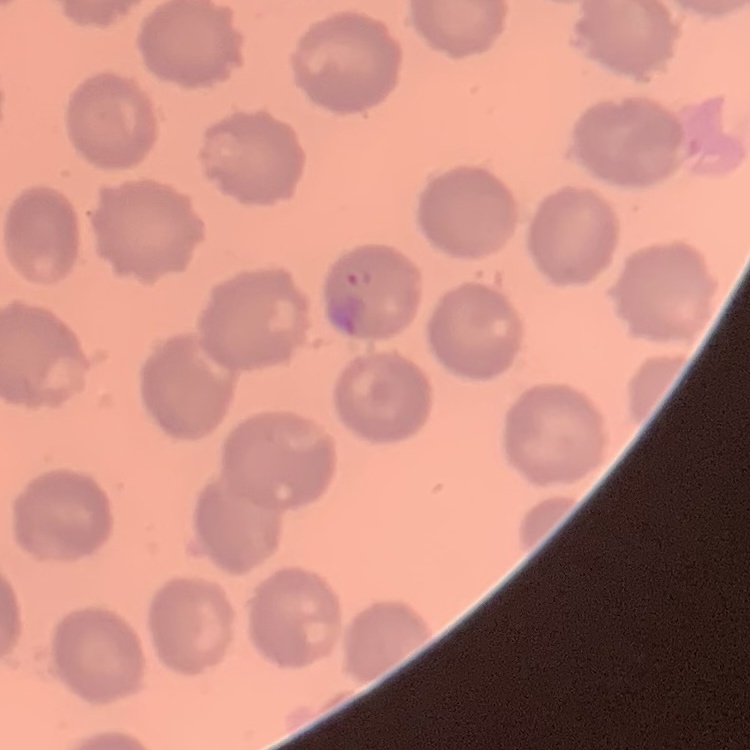 The erythrocytes exhibit no rouleaux formation. Square crop of a larger photomicrograph. Stained with either Field's or Giemsa. Thin blood smear.